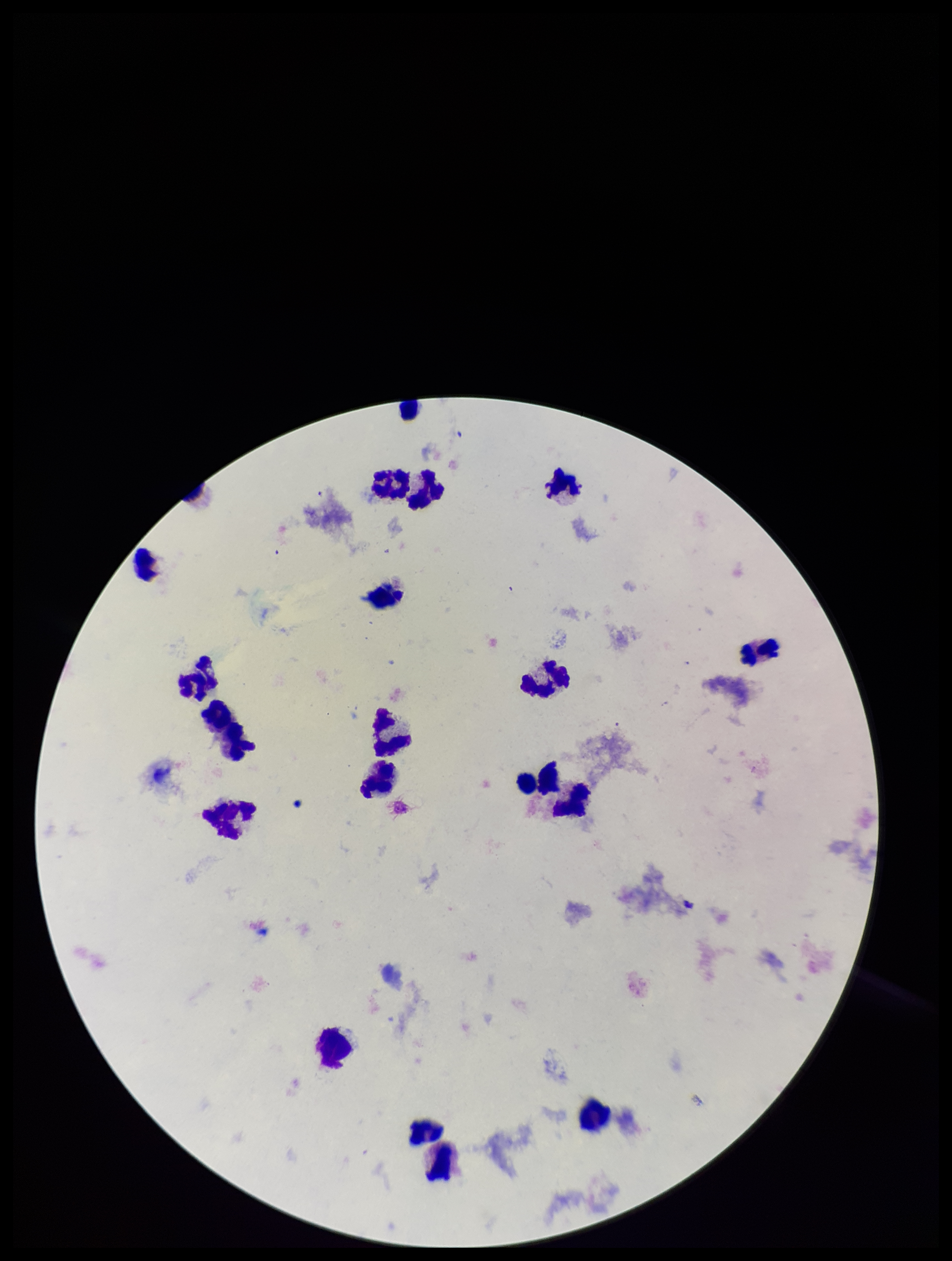
field of view = single
capture = smartphone photograph through the microscope eyepiece
parasite count = 0
stain = Giemsa
Plasmodium parasites = none seen
patient malaria status = negative
image size = 952×1261 pixels
leukocyte count = 19
preparation = thick